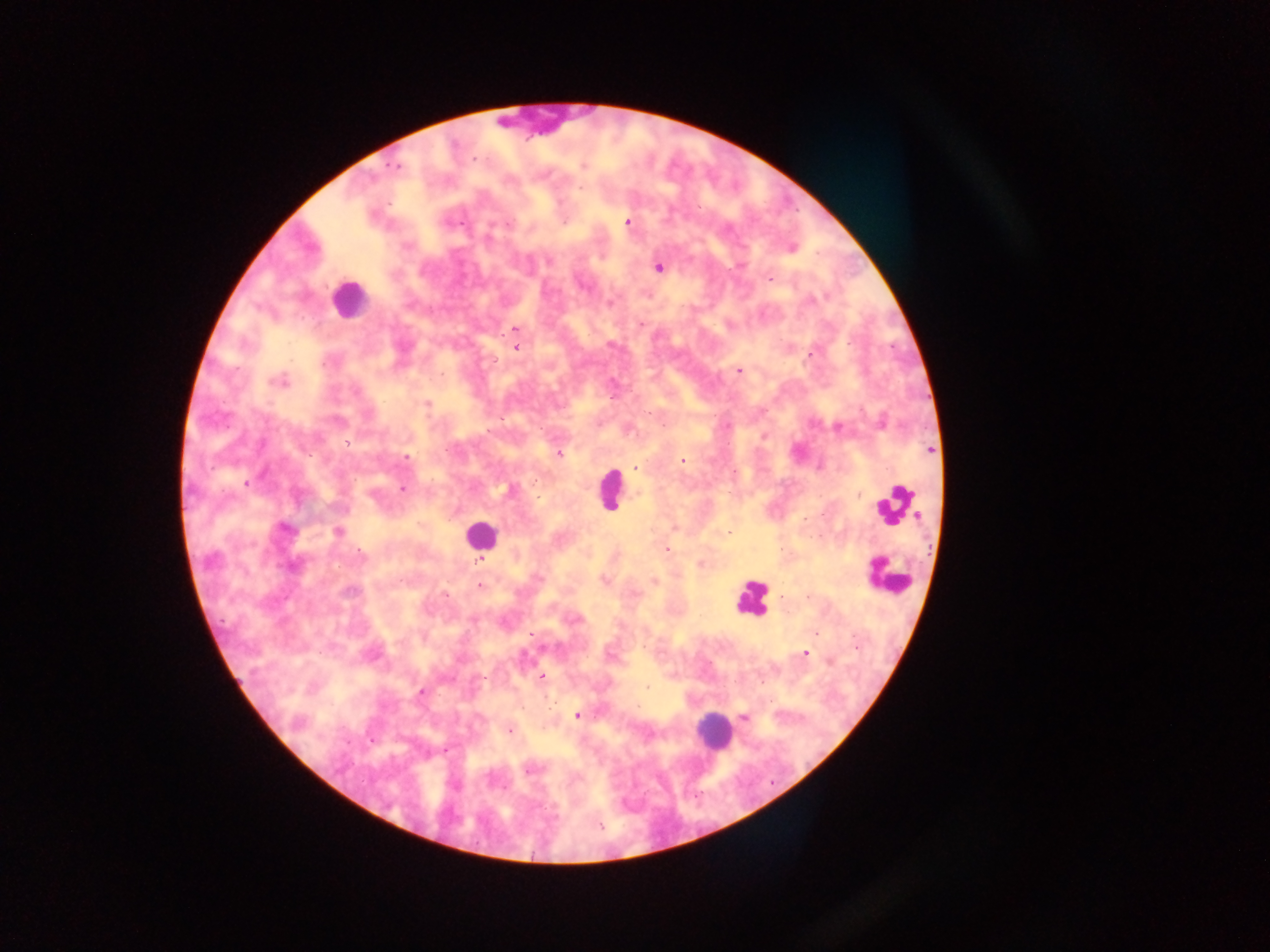

Approximate centers as (x, y) in pixels. Plasmodium parasite locations: (475, 159), (393, 166), (583, 166), (627, 222), (462, 223), (508, 223), (488, 238), (549, 261), (658, 268), (770, 278), (812, 299), (610, 302), (640, 325), (515, 330), (850, 343), (517, 348), (810, 355), (739, 371), (443, 375), (279, 382), (614, 397), (427, 404), (727, 425), (838, 427), (763, 437), (347, 442), (930, 451), (558, 453), (407, 458), (682, 461), (635, 468), (246, 483), (403, 489), (371, 493), (859, 494), (285, 529), (338, 532), (728, 532), (667, 549), (362, 554), (210, 560), (480, 561), (701, 563), (291, 565), (605, 580), (654, 581), (480, 586), (350, 591), (446, 596), (808, 597), (473, 621), (816, 633), (530, 634), (855, 647), (805, 653), (541, 676), (646, 687), (421, 692), (577, 715), (745, 717), (510, 730), (445, 751), (528, 770), (601, 826). Leukocyte locations: (541, 117), (349, 299), (611, 489), (896, 506), (480, 535), (888, 576), (751, 598), (713, 730). Image is 1270×952 pixels. One field of view. Sample from Ghana. Photographed through a microscope with a mobile-phone camera. Thick blood smear.